Assess this cell for malaria.
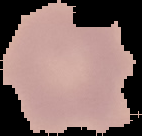
It is uninfected.

Image is 142×136 pixels. From a thin blood film. The area outside the segmented cell region is set to black.